Comment on the morphology of the red blood cells.
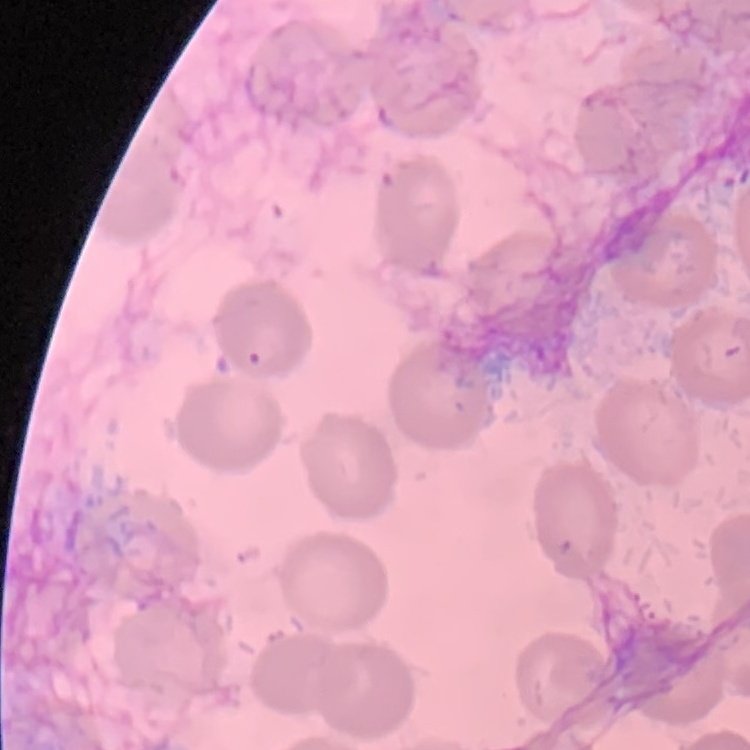
They show no rouleaux formation.

Thin peripheral smear. One tile cut from a larger photomicrograph. Stained with either Field's or Giemsa.